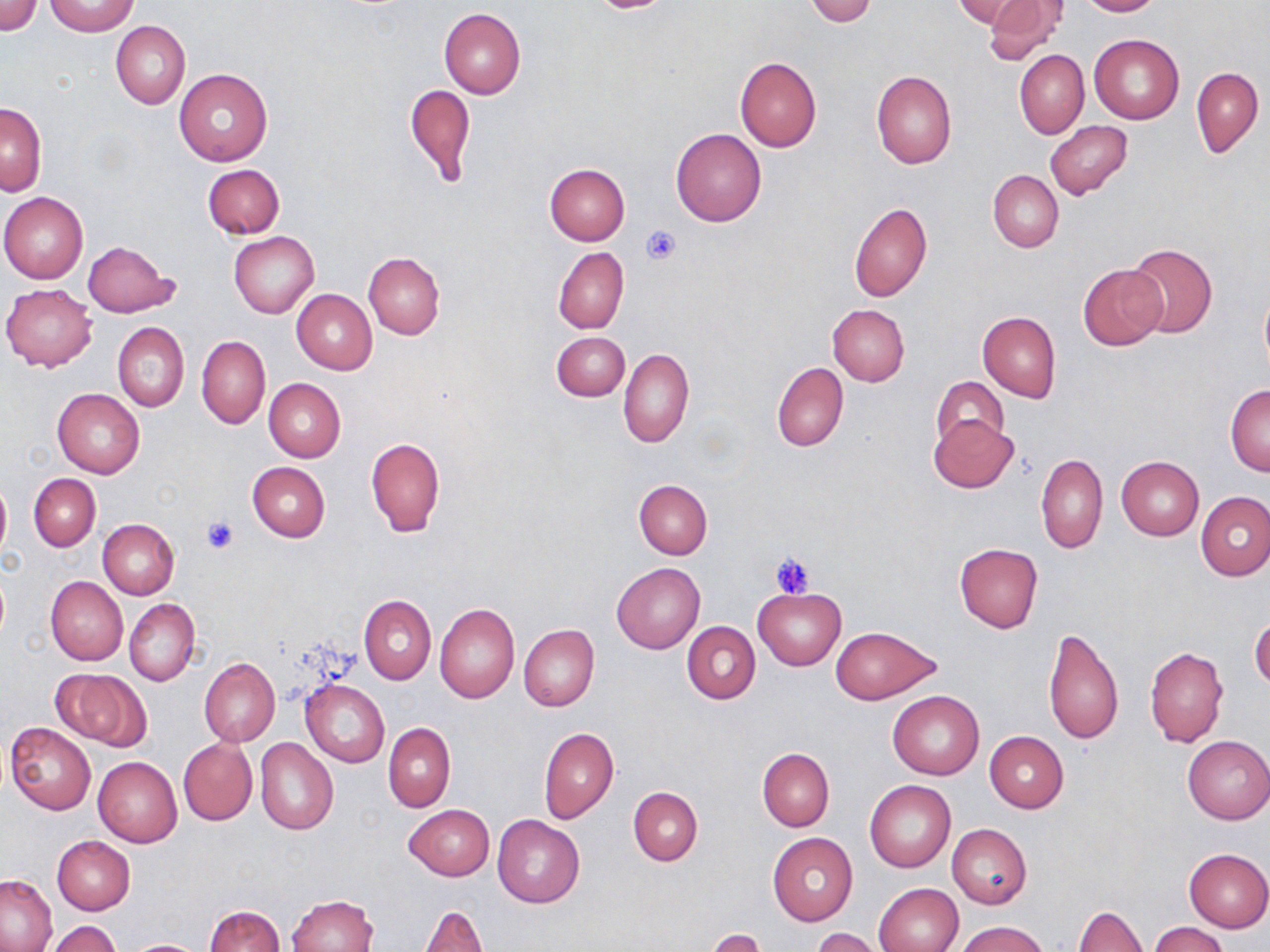

Summary:
  - Coordinate format: approximate bounding boxes as [x1, y1, x2, y2] in pixels
  - Platelet locations: [642, 225, 682, 267], [200, 515, 239, 554], [770, 552, 816, 597]
  - Uninfected red blood cell locations: [0, 0, 41, 36], [805, 0, 880, 26], [982, 0, 1064, 64], [1077, 0, 1160, 16], [953, 1, 1028, 29], [46, 2, 139, 36], [439, 8, 525, 98], [111, 21, 190, 108], [1090, 34, 1184, 125], [1015, 49, 1089, 138], [734, 57, 822, 152], [1192, 67, 1263, 156], [175, 69, 271, 166], [871, 70, 957, 169], [405, 83, 475, 185], [1, 102, 46, 196], [1044, 121, 1132, 199], [670, 128, 766, 227], [544, 163, 631, 244], [202, 164, 285, 238], [988, 170, 1063, 252], [0, 192, 89, 283], [849, 202, 932, 303], [230, 232, 319, 318], [82, 240, 179, 318], [1124, 242, 1217, 339], [553, 247, 629, 334], [363, 251, 445, 340], [1079, 264, 1167, 350], [1, 283, 98, 372], [292, 289, 377, 374], [1259, 289, 1270, 377], [827, 304, 909, 386], [978, 311, 1061, 402], [114, 323, 189, 414], [551, 331, 630, 402], [196, 335, 270, 429], [619, 348, 694, 447], [772, 362, 848, 452], [932, 376, 1008, 451], [264, 378, 346, 463], [1226, 385, 1270, 476], [52, 388, 144, 478], [929, 415, 1017, 493], [366, 436, 446, 536], [1035, 453, 1108, 554], [1116, 456, 1204, 540], [246, 462, 331, 542], [29, 474, 100, 551], [0, 475, 11, 568], [633, 479, 712, 559], [1195, 491, 1270, 581], [98, 519, 179, 599], [954, 543, 1043, 632], [611, 561, 706, 654], [45, 576, 128, 666], [753, 588, 845, 669], [359, 595, 436, 684], [125, 598, 199, 686], [434, 603, 519, 703], [1250, 616, 1270, 689], [682, 621, 761, 704], [519, 624, 600, 710], [830, 626, 939, 704], [1043, 627, 1124, 746], [1145, 646, 1227, 747], [200, 658, 280, 746], [54, 668, 150, 750], [300, 680, 389, 767], [887, 689, 984, 780], [5, 721, 96, 814], [383, 722, 455, 812], [539, 727, 619, 824], [984, 731, 1069, 812], [1182, 735, 1269, 824], [178, 738, 257, 826], [256, 738, 338, 835], [757, 748, 835, 830], [93, 755, 182, 847], [864, 780, 955, 872], [628, 787, 702, 866], [404, 804, 495, 881], [492, 814, 585, 908], [947, 823, 1033, 909], [768, 833, 858, 925], [51, 837, 134, 915], [1184, 848, 1270, 931], [0, 874, 58, 951], [874, 882, 962, 952], [288, 894, 378, 952], [205, 904, 284, 952], [416, 905, 488, 952], [1073, 906, 1148, 952], [45, 921, 122, 952], [958, 921, 1046, 952], [1150, 922, 1228, 952], [704, 928, 767, 952], [812, 928, 885, 952], [124, 939, 211, 952]
  - Slide-level diagnosis: no evidence of blood parasites
  - Image size: 1270×952 pixels
  - Field of view: single
  - Preparation: thin blood smear
  - Magnification: 1000x
  - Stain: May-Grünwald-Giemsa
  - Modality: light microscopy